Classify this cell by malaria status.
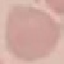

Uninfected.

capture = smartphone through the microscope eyepiece
stain = Giemsa
preparation = thin blood smear
image type = cell patch, automatically extracted from a larger field of view and resized to 64 × 64 pixels